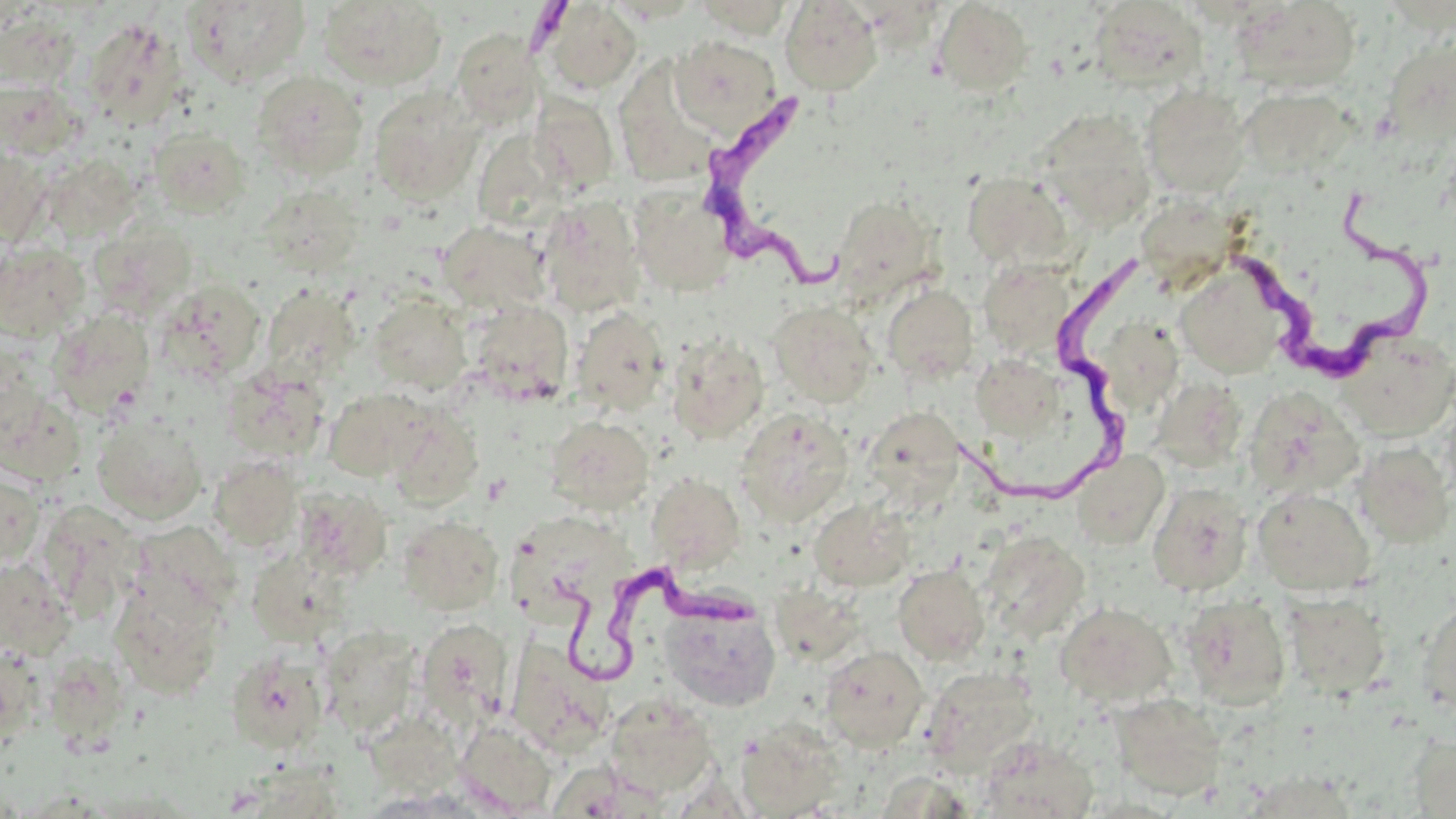

Summary:
  - Coordinate format: approximate bounding boxes as [x1, y1, x2, y2] in pixels
  - Uninfected red blood cell locations: [317, 0, 447, 90], [780, 0, 883, 95], [184, 1, 311, 86], [685, 1, 798, 38], [1089, 1, 1209, 92], [1234, 1, 1360, 94], [540, 2, 642, 94], [933, 2, 1033, 96], [1, 9, 83, 91], [83, 18, 186, 129], [452, 28, 542, 125], [670, 35, 782, 135], [1392, 46, 1455, 147], [252, 70, 368, 179], [625, 76, 717, 182], [0, 79, 82, 159], [1140, 85, 1251, 198], [368, 86, 483, 204], [1238, 87, 1357, 178], [530, 93, 619, 193], [1034, 108, 1156, 231], [148, 126, 250, 218], [0, 147, 51, 245], [40, 155, 140, 243], [962, 172, 1074, 271], [259, 184, 366, 278], [629, 184, 736, 297], [538, 197, 645, 318], [830, 197, 939, 303], [437, 220, 551, 316], [0, 241, 91, 341], [978, 258, 1076, 362], [1174, 263, 1287, 378], [157, 278, 267, 382], [260, 284, 361, 381], [882, 285, 977, 384], [368, 294, 470, 393], [466, 299, 573, 402], [768, 301, 876, 407], [572, 307, 669, 415], [46, 310, 155, 420], [1103, 324, 1185, 412], [1335, 331, 1456, 439], [666, 335, 769, 444], [970, 355, 1062, 440], [222, 365, 329, 463], [1, 385, 85, 487], [1242, 387, 1364, 500], [323, 388, 431, 480], [1160, 389, 1243, 470], [1440, 401, 1456, 506], [865, 406, 963, 503], [734, 408, 853, 525], [386, 409, 483, 508], [93, 413, 207, 525], [546, 416, 655, 514], [1354, 441, 1454, 548], [1072, 451, 1170, 550], [210, 455, 303, 550], [0, 470, 45, 570], [647, 473, 744, 572], [1147, 482, 1253, 596], [1268, 486, 1381, 700], [1253, 487, 1374, 595], [809, 498, 914, 591], [35, 501, 145, 618], [397, 514, 503, 614], [511, 517, 634, 623], [978, 529, 1090, 644], [0, 560, 76, 660], [893, 564, 990, 664], [110, 575, 227, 699], [764, 588, 858, 660], [1283, 593, 1391, 698], [1181, 596, 1291, 709], [1416, 596, 1456, 718], [1055, 601, 1177, 707], [661, 603, 781, 711], [416, 617, 514, 728], [318, 625, 422, 738], [516, 633, 607, 750], [0, 643, 44, 745], [820, 645, 929, 751], [226, 649, 330, 754], [43, 652, 130, 745], [920, 665, 1041, 774], [604, 693, 717, 798], [1110, 693, 1226, 801], [737, 719, 846, 817], [455, 720, 558, 816], [1409, 732, 1456, 818], [975, 736, 1099, 818]
  - Trypanosoma brucei locations: [696, 85, 851, 292], [1233, 190, 1420, 375], [960, 253, 1149, 511], [544, 557, 761, 683]
  - Slide-level diagnosis: Trypanosoma brucei
  - Modality: optical microscopy
  - Stain: May-Grünwald-Giemsa
  - Field of view: one of a larger specimen
  - Magnification: 1000x
  - Image size: 1456×819 pixels
  - Preparation: thin blood smear